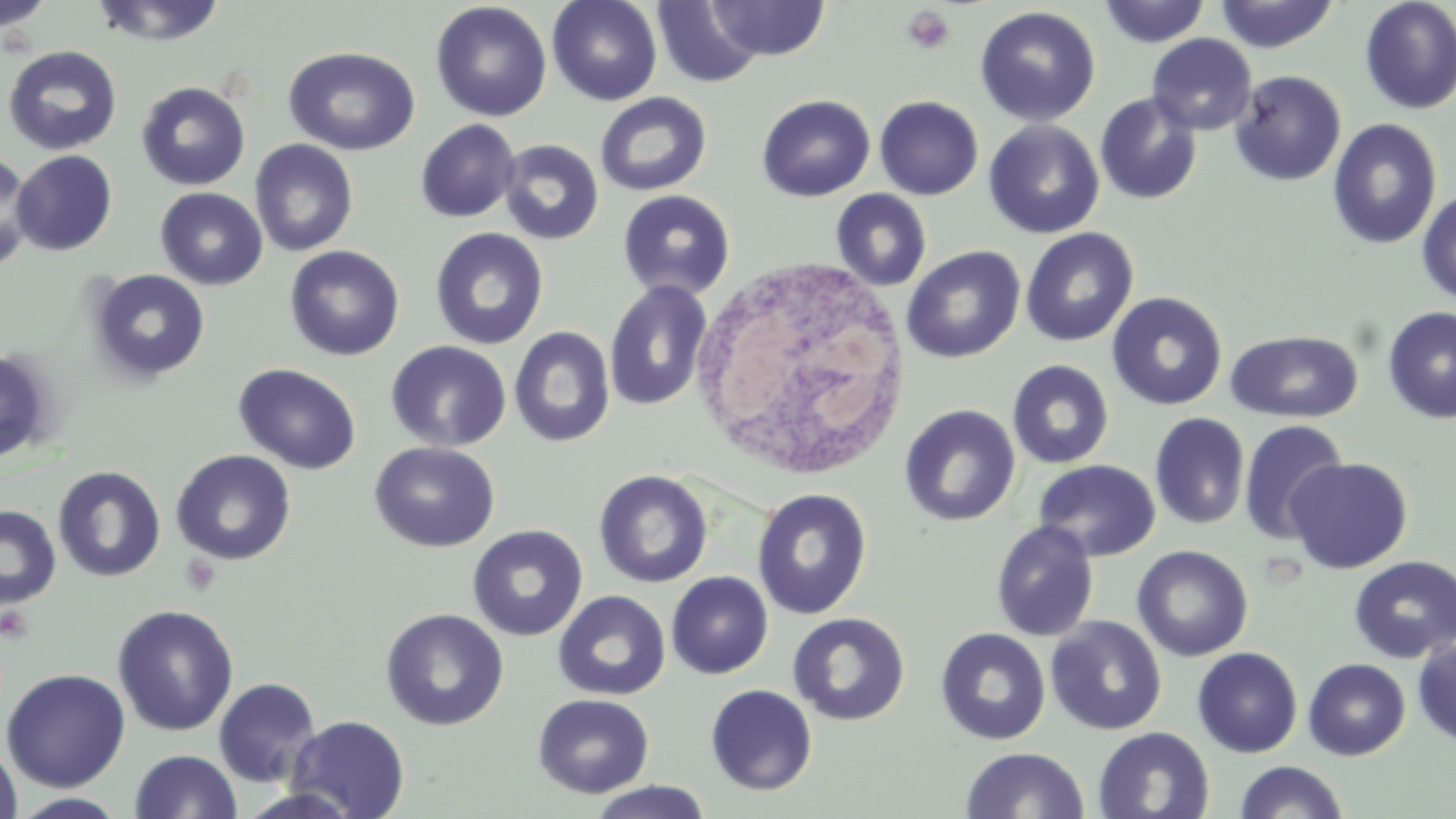

{
  "slide_level_diagnosis": "negative for blood parasites",
  "modality": "optical microscopy",
  "field_of_view": "single",
  "stain": "May-Grünwald-Giemsa",
  "image_size": "1456×819 pixels",
  "uninfected_red_blood_cell_locations": "approximate bounding boxes as (x1,y1)-(x2,y2) corner pairs in pixels: (0,0)-(56,34), (90,0)-(228,47), (547,0)-(662,106), (651,0)-(767,88), (1098,0)-(1211,47), (707,1)-(830,61), (1214,1)-(1341,53), (1359,1)-(1456,114), (430,2)-(552,122), (975,6)-(1101,127), (1147,34)-(1257,135), (2,45)-(122,156), (283,46)-(420,156), (1229,70)-(1346,186), (136,81)-(250,191), (595,92)-(712,197), (1094,92)-(1203,205), (756,95)-(875,202), (875,95)-(984,200), (1327,118)-(1442,250), (416,119)-(521,222), (984,120)-(1105,239), (250,139)-(358,256), (498,139)-(604,245), (11,151)-(117,255), (1,154)-(36,271), (155,188)-(268,290), (1416,188)-(1456,305), (617,189)-(736,300), (830,189)-(932,292), (429,227)-(549,350), (1020,228)-(1139,347), (284,245)-(404,361), (902,245)-(1025,363), (87,269)-(211,385), (604,280)-(713,411), (1106,291)-(1227,411), (1381,306)-(1456,425), (509,326)-(616,447), (1225,330)-(1363,423), (386,340)-(512,453), (0,347)-(54,464), (1006,359)-(1115,469), (233,362)-(362,474), (899,404)-(1020,526), (1149,412)-(1250,530), (1238,418)-(1350,545), (369,441)-(500,553), (170,449)-(297,565), (1284,456)-(1413,574), (1033,459)-(1161,562), (52,466)-(166,582), (593,470)-(713,588), (751,487)-(872,620), (0,504)-(61,610), (990,520)-(1099,642), (467,524)-(588,641), (1132,544)-(1253,662), (1349,555)-(1456,662), (666,572)-(773,679), (553,590)-(670,701), (112,604)-(239,736), (380,608)-(509,731), (788,612)-(911,725), (1045,616)-(1167,735), (935,627)-(1051,745), (1412,637)-(1456,747), (1192,647)-(1303,757), (1303,658)-(1410,760), (2,668)-(131,792), (214,677)-(321,788), (705,684)-(818,796), (533,693)-(654,799), (286,715)-(410,818), (1093,726)-(1214,818), (0,740)-(22,819), (960,747)-(1089,819), (130,749)-(242,819), (1234,760)-(1349,819), (586,781)-(713,819), (8,792)-(130,818)",
  "magnification": "1000x",
  "platelet_locations": "approximate bounding boxes as (x1,y1)-(x2,y2) corner pairs in pixels: (901,5)-(956,55)",
  "white_blood_cell_locations": "approximate bounding boxes as (x1,y1)-(x2,y2) corner pairs in pixels: (688,253)-(913,481)",
  "preparation": "thin blood smear"
}